Classify this cell by malaria status.
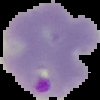
Parasitized.

{
  "image_size": "100×100 pixels",
  "preparation": "thin blood film",
  "image_type": "cell region segmented out of the field of view; surrounding area masked to black"
}